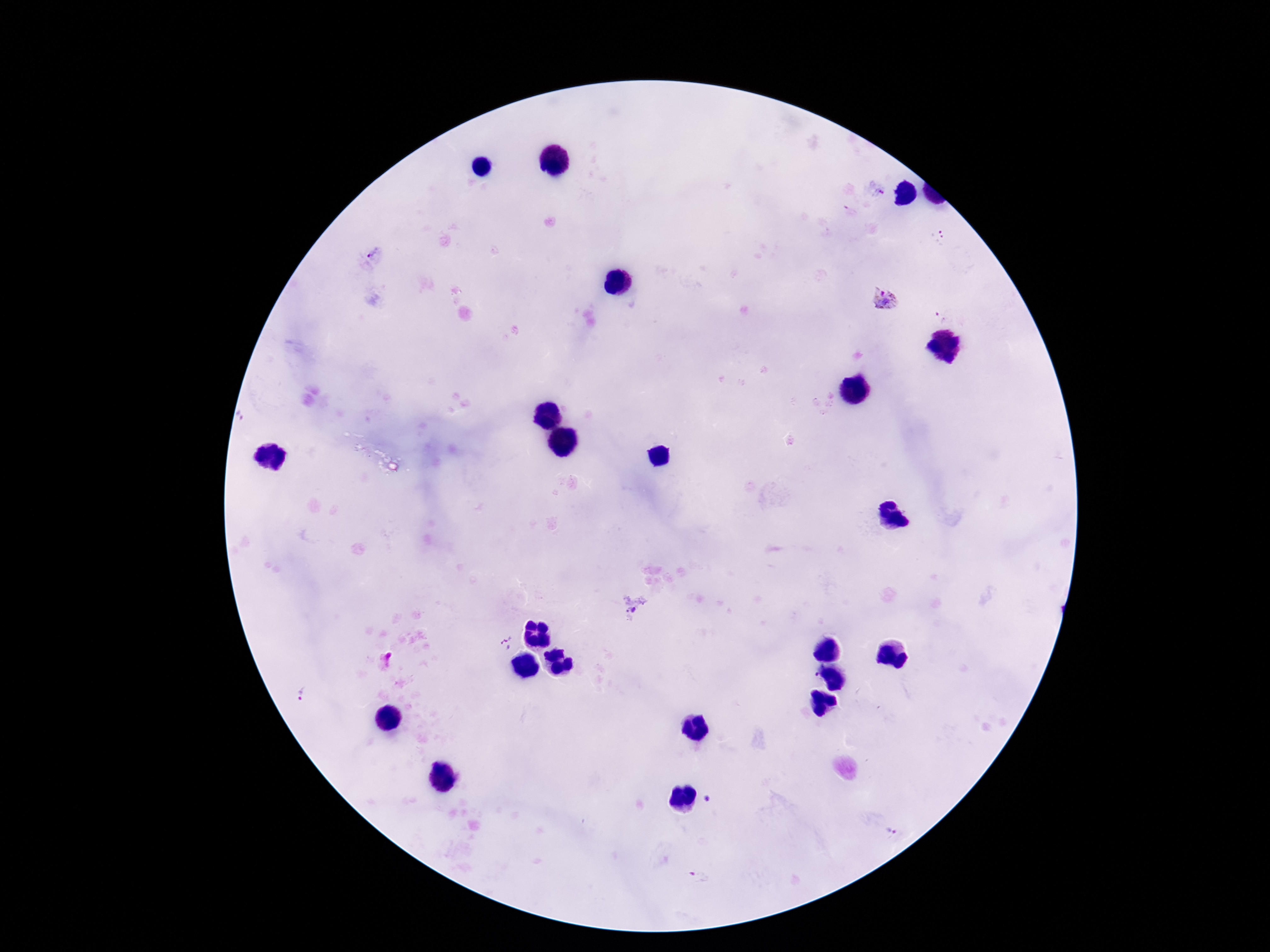

stain = Giemsa
magnification = 100x
capture = smartphone camera through the microscope eyepiece
patient malaria status = positive
preparation = thick blood smear
image size = 1270×952 pixels
field of view = one from this slide
Plasmodium parasite locations = approximate centers as [x, y] in pixels: [876, 189], [938, 236], [886, 298], [942, 314], [634, 610], [506, 643], [303, 696], [708, 799], [890, 833], [699, 876]